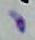

modality = micrograph
identification = Toxoplasma gondii
magnification = 1000x